Name the parasite shown.
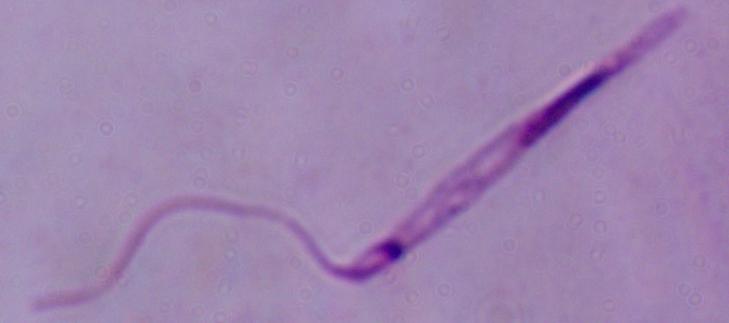
Leishmania.

Micrograph. Captured at 1000x magnification.